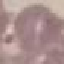

Summary:
  - Result: negative for malaria parasites
  - Preparation: thin blood film
  - Image type: cell patch, automatically extracted from a larger field of view and resized to 64 × 64 pixels
  - Stain: Giemsa
  - Capture: smartphone camera at the microscope eyepiece